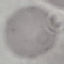
malaria status = uninfected
capture = smartphone camera at the microscope eyepiece
stain = Giemsa
image type = cell patch, automatically extracted from a larger field of view and resized to 64 × 64 pixels
preparation = thin blood smear